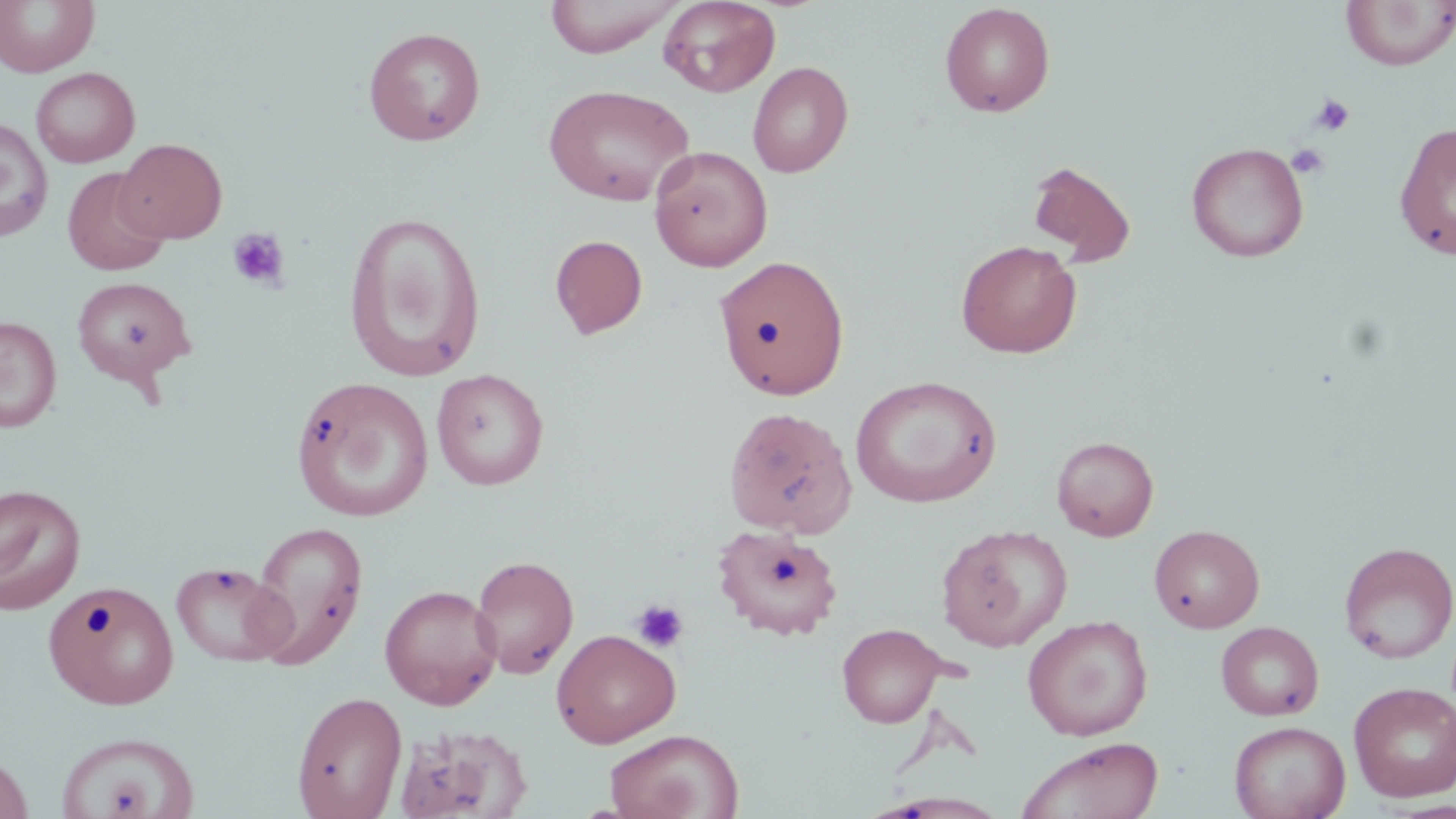
Summary:
  - Coordinate format: approximate bounding boxes as (x1, y1, x2, y2) in pixels
  - Platelet locations: (1311, 93, 1355, 136), (1286, 143, 1330, 179), (227, 228, 290, 291), (631, 600, 689, 653)
  - Uninfected red blood cell locations: (0, 0, 99, 77), (544, 0, 682, 57), (658, 0, 780, 96), (1341, 1, 1456, 70), (939, 2, 1055, 117), (363, 26, 486, 146), (748, 61, 854, 178), (30, 67, 140, 167), (543, 84, 695, 207), (0, 118, 54, 242), (1394, 121, 1456, 261), (115, 138, 227, 244), (1187, 142, 1309, 262), (649, 146, 773, 272), (1027, 160, 1136, 266), (62, 167, 170, 277), (342, 211, 487, 381), (550, 234, 648, 339), (955, 239, 1082, 358), (714, 254, 850, 400), (71, 275, 196, 388), (0, 316, 61, 432), (431, 368, 549, 490), (851, 375, 1002, 508), (292, 376, 434, 522), (723, 406, 858, 537), (1051, 435, 1159, 541), (0, 484, 86, 614), (250, 520, 368, 668), (937, 524, 1073, 652), (1149, 524, 1265, 633), (712, 525, 844, 641), (1338, 540, 1455, 664), (470, 554, 579, 679), (170, 560, 293, 666), (43, 582, 181, 710), (379, 584, 502, 709), (1022, 615, 1153, 741), (1216, 621, 1324, 720), (837, 623, 945, 728), (551, 628, 680, 747), (1349, 680, 1456, 803), (291, 690, 407, 819), (1229, 720, 1350, 819), (392, 725, 532, 819), (604, 728, 744, 819), (53, 731, 199, 819), (1015, 736, 1165, 819), (0, 754, 34, 819), (865, 792, 1012, 818)
  - Slide-level diagnosis: no evidence of blood parasites
  - Field of view: single
  - Magnification: 1000x
  - Stain: May-Grünwald-Giemsa
  - Preparation: thin blood smear
  - Modality: optical microscopy
  - Image size: 1456×819 pixels